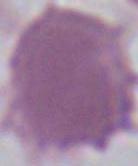 Micrograph. Captured at 1000x magnification. An erythrocyte is shown.